Report the malaria status of this cell.
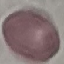
Uninfected.

Summary:
  - Stain: Giemsa
  - Capture: smartphone camera at the microscope eyepiece
  - Image type: cell patch, automatically extracted from a larger field of view and resized to 64 × 64 pixels
  - Preparation: thin smear